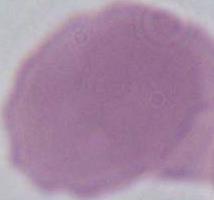

{
  "magnification": "1000x",
  "identification": "red blood cell",
  "modality": "photomicrograph"
}